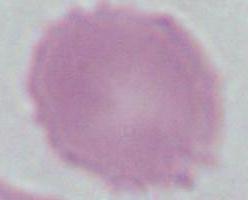
Summary:
  - Identification: red blood cell
  - Magnification: 1000x
  - Modality: micrograph